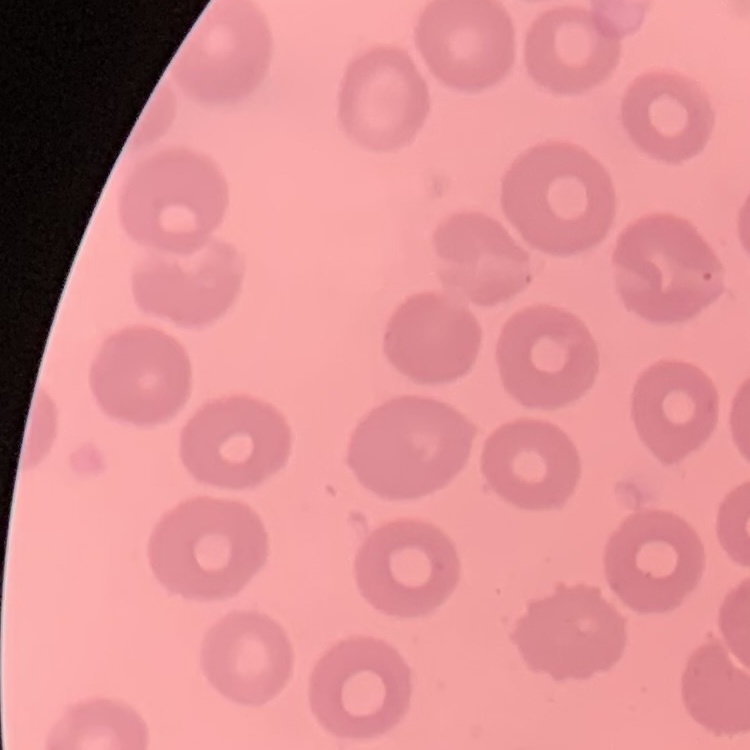
Summary:
  - Erythrocyte morphology: no rouleaux formation
  - Preparation: thin blood smear
  - Image type: square crop of a larger photomicrograph
  - Stain: Field's or Giemsa